Name the cell type shown.
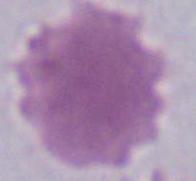
This is an erythrocyte.

Micrograph. 1000x magnification.